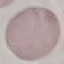

malaria status = uninfected
capture = smartphone camera at the microscope eyepiece
image type = cell patch, automatically extracted from a larger field of view and resized to 64 × 64 pixels
preparation = thin smear
stain = Giemsa